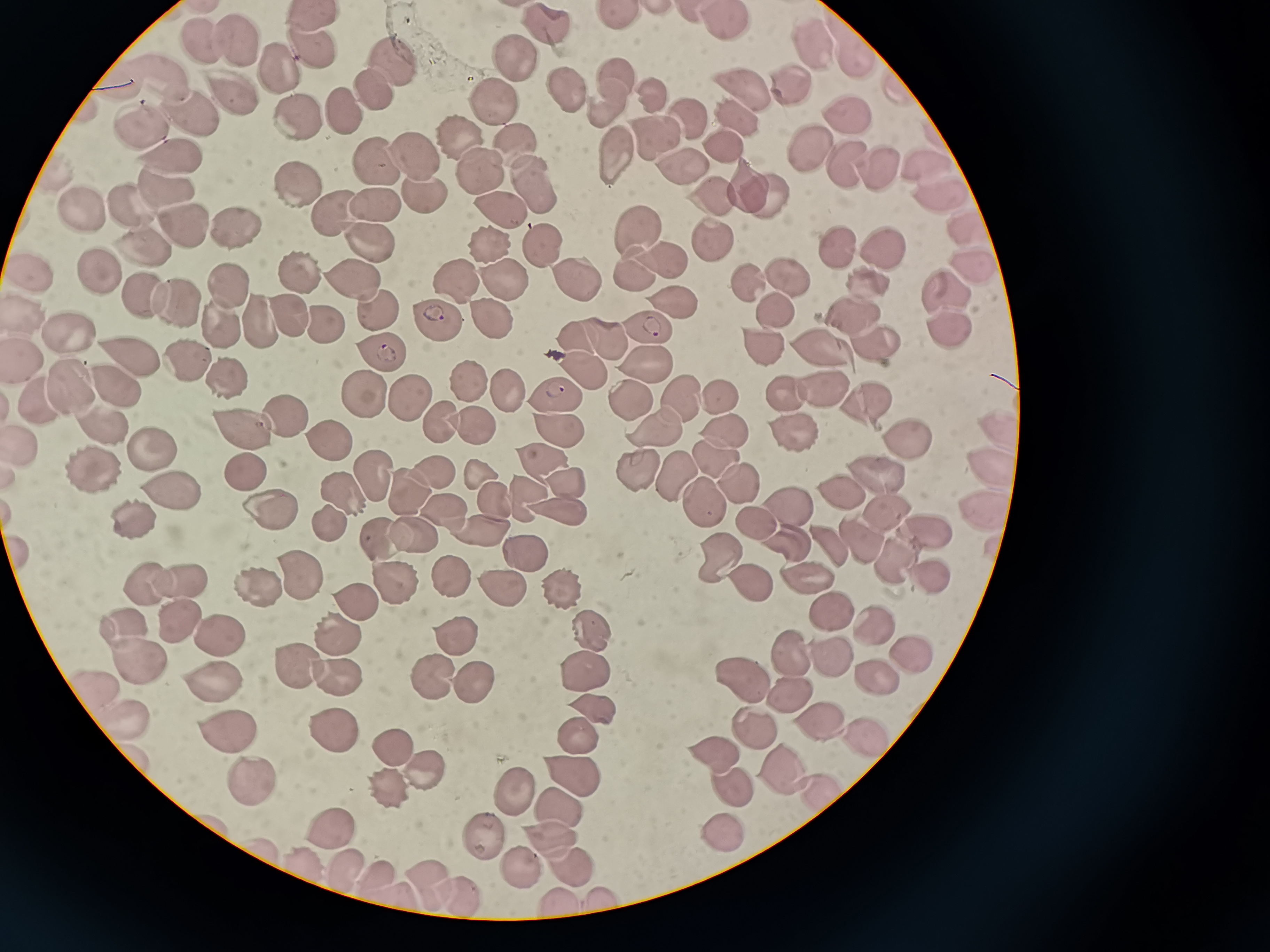 Approximate centers as [x, y] in pixels. Cell locations: [619, 16], [309, 20], [543, 25], [726, 26], [237, 42], [200, 44], [810, 45], [311, 47], [854, 53], [391, 60], [512, 65], [280, 70], [618, 78], [160, 80], [792, 81], [563, 88], [741, 88], [370, 90], [230, 92], [653, 100], [493, 101], [341, 105], [604, 105], [189, 114], [297, 114], [847, 114], [740, 116], [690, 117], [137, 122], [653, 134], [455, 137], [513, 143], [728, 143], [413, 152], [810, 152], [614, 153], [375, 161], [681, 161], [930, 161], [172, 162], [880, 163], [843, 164], [479, 170], [534, 178], [300, 179], [748, 186], [167, 189], [422, 190], [712, 190], [768, 190], [939, 192], [378, 204], [125, 205], [501, 207], [78, 209], [333, 210], [965, 220], [233, 225], [184, 226], [636, 232], [369, 236], [708, 240], [547, 242], [487, 245], [840, 246], [883, 247], [141, 250], [659, 256], [972, 263], [98, 267], [31, 270], [629, 272], [785, 273], [300, 274], [568, 274], [454, 276], [862, 277], [499, 279], [748, 279], [355, 281], [228, 284], [946, 285], [142, 290], [177, 297], [669, 301], [377, 304], [775, 306], [853, 311], [290, 314], [27, 317], [259, 319], [439, 319], [490, 320], [220, 321], [320, 324], [646, 326], [947, 326], [575, 336], [603, 336], [68, 337], [876, 338], [766, 342], [826, 345], [382, 346], [132, 355], [186, 356], [645, 360], [28, 361], [223, 369], [581, 369], [465, 378], [113, 388], [500, 388], [820, 389], [68, 390], [363, 391], [684, 391], [721, 391], [783, 391], [411, 394], [554, 395], [865, 399], [624, 400], [37, 406], [284, 414], [437, 419], [471, 424], [241, 425], [998, 425], [103, 427], [657, 427], [556, 428], [790, 430], [727, 433], [904, 433], [326, 439], [26, 445], [155, 449], [538, 457], [717, 460], [673, 467], [992, 467], [95, 469], [245, 469], [429, 469], [638, 469], [478, 472], [877, 472], [369, 475], [566, 479], [738, 481], [403, 490], [839, 490], [522, 491], [699, 495], [173, 497], [342, 497], [492, 497], [788, 501], [266, 505], [436, 507], [886, 508], [555, 509], [982, 510], [128, 513], [325, 521], [757, 521], [927, 527], [484, 533], [414, 535], [382, 538], [858, 538], [785, 540], [831, 544], [524, 553], [717, 555], [886, 555], [453, 570], [806, 572], [299, 577], [925, 578], [747, 580], [180, 581], [503, 582], [392, 583], [146, 584], [563, 586], [256, 587], [358, 598], [829, 605], [184, 617], [872, 618], [578, 621], [123, 623], [460, 630], [223, 633], [338, 633], [910, 648], [792, 654], [833, 658], [135, 661], [297, 664], [580, 670], [881, 671], [430, 675], [338, 676], [744, 677], [466, 678], [206, 680], [100, 684], [784, 689], [592, 704], [117, 721], [755, 723], [816, 725], [330, 728], [578, 730], [228, 737], [859, 737], [389, 739], [719, 753], [135, 758], [419, 764], [780, 764], [572, 771], [254, 782], [724, 782], [389, 785], [514, 786], [822, 795], [555, 810], [336, 823], [478, 829], [718, 829], [549, 843], [345, 862], [571, 866], [516, 869], [373, 872], [429, 880], [457, 893], [398, 900], [559, 905]. Thin blood smear. Giemsa stain. Image is 1270×952 pixels. One field from this slide. Photographed with a smartphone camera at the microscope eyepiece.